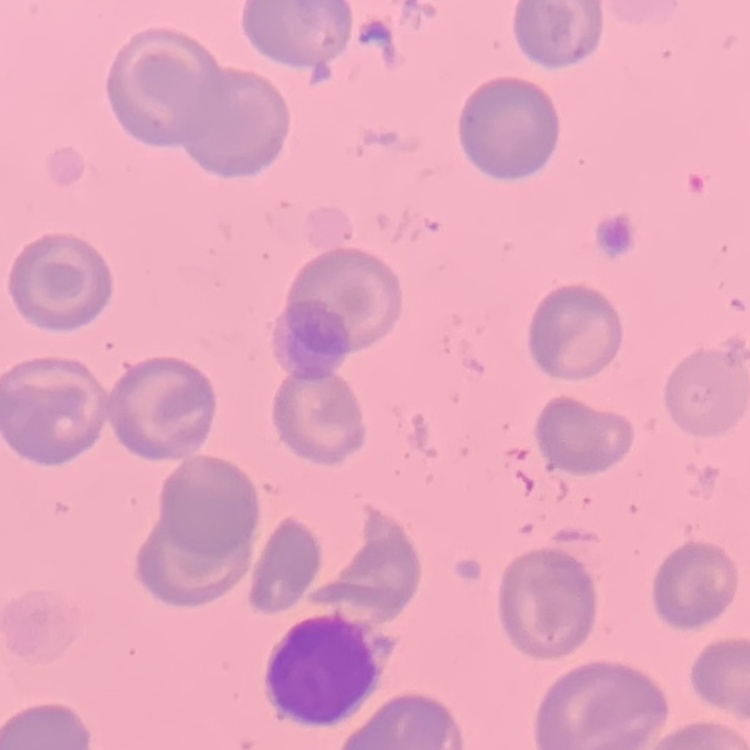

The red blood cells exhibit no rouleaux formation. Thin blood smear. Stained with either Field's or Giemsa. One tile cut from a larger photomicrograph.